Locate and identify every blood parasite.
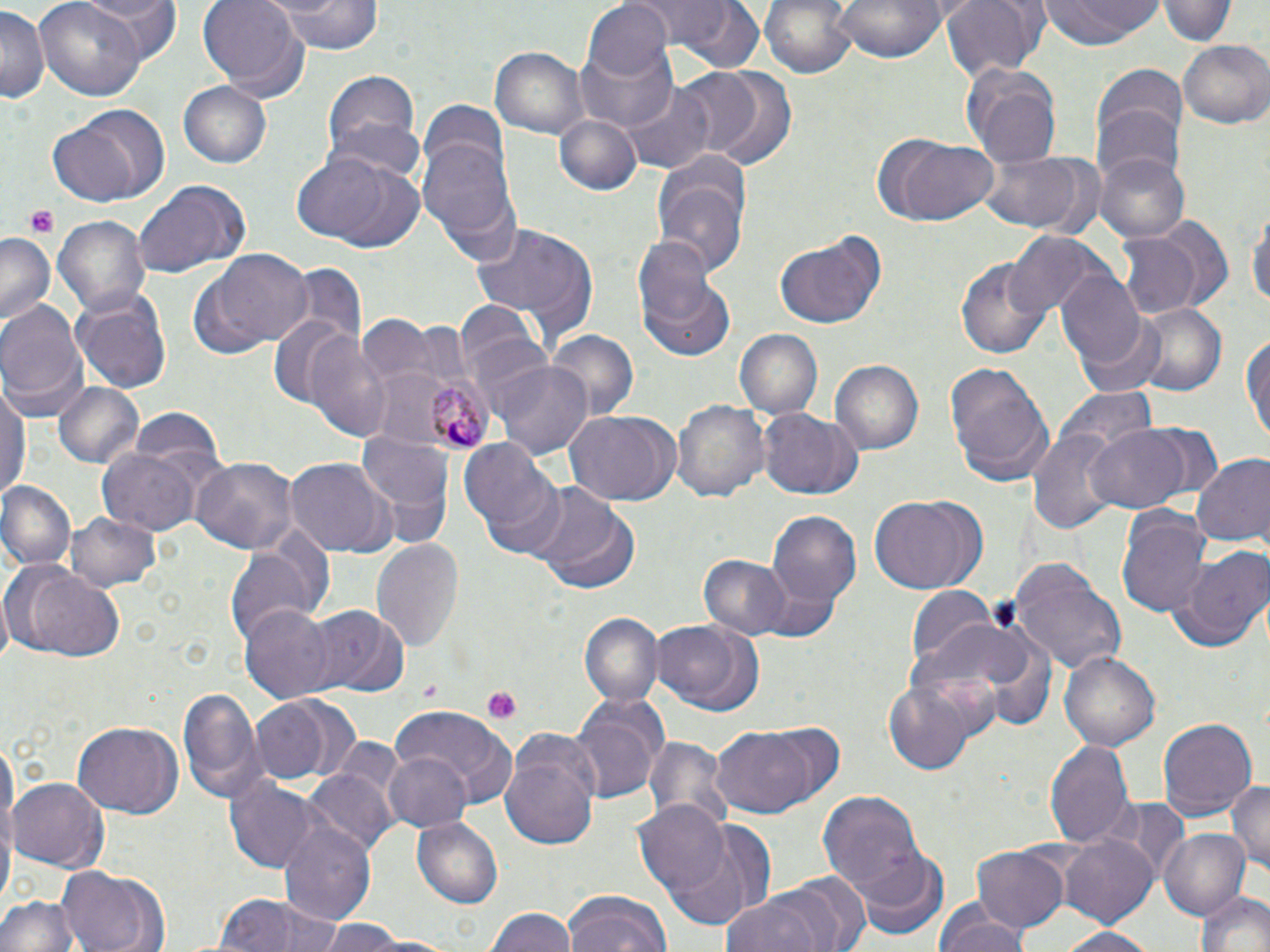

Approximate bounding boxes as [x1, y1, x2, y2] in pixels.
Plasmodium malariae-infected red blood cells: [425, 375, 491, 451].
No Plasmodium falciparum, Plasmodium ovale, Plasmodium vivax, Babesia divergens, or Trypanosoma brucei observed.

Summary:
  - Platelet locations: [25, 205, 61, 236], [478, 685, 525, 726]
  - Uninfected red blood cell locations: [33, 0, 144, 99], [80, 0, 181, 66], [198, 0, 308, 100], [269, 0, 386, 56], [582, 0, 677, 83], [622, 0, 762, 60], [758, 0, 859, 80], [832, 0, 951, 62], [941, 0, 1040, 80], [1040, 0, 1164, 49], [1160, 0, 1236, 47], [0, 9, 45, 102], [577, 40, 680, 132], [1180, 40, 1270, 129], [490, 46, 588, 139], [961, 63, 1061, 164], [674, 66, 767, 158], [1090, 66, 1187, 152], [322, 68, 420, 169], [704, 68, 799, 172], [622, 80, 715, 173], [179, 81, 270, 168], [421, 99, 512, 189], [50, 103, 170, 204], [1091, 105, 1185, 191], [553, 112, 642, 196], [417, 135, 520, 254], [877, 135, 999, 226], [291, 148, 417, 250], [1097, 152, 1192, 244], [977, 153, 1100, 236], [654, 154, 752, 273], [133, 180, 248, 277], [1248, 207, 1269, 321], [54, 215, 151, 320], [1155, 217, 1230, 306], [470, 223, 595, 328], [774, 228, 889, 330], [1116, 232, 1200, 318], [1007, 233, 1106, 323], [0, 235, 53, 324], [633, 237, 718, 327], [198, 250, 314, 351], [954, 254, 1053, 360], [638, 266, 738, 367], [1057, 274, 1146, 367], [72, 292, 172, 396], [0, 299, 86, 414], [456, 301, 547, 386], [1133, 302, 1226, 394], [268, 311, 359, 410], [358, 315, 432, 391], [1073, 315, 1167, 397], [1242, 328, 1270, 449], [737, 329, 823, 418], [546, 330, 637, 421], [307, 332, 389, 440], [491, 359, 593, 459], [832, 360, 922, 456], [946, 362, 1056, 485], [1, 378, 30, 502], [54, 383, 144, 468], [1053, 387, 1156, 456], [671, 397, 771, 506], [130, 406, 225, 478], [757, 409, 861, 500], [564, 412, 679, 504], [1135, 422, 1224, 504], [1028, 424, 1125, 536], [1083, 424, 1192, 514], [356, 430, 452, 535], [460, 437, 568, 560], [98, 447, 199, 536], [191, 456, 300, 554], [1191, 456, 1269, 549], [285, 458, 392, 557], [0, 481, 76, 571], [527, 482, 639, 594], [869, 493, 979, 595], [1117, 505, 1212, 617], [67, 511, 163, 593], [769, 512, 863, 609], [372, 536, 466, 654], [224, 541, 324, 652], [1168, 543, 1268, 652], [700, 554, 794, 638], [1010, 558, 1128, 674], [14, 565, 127, 665], [909, 587, 999, 671], [240, 603, 338, 703], [305, 605, 411, 698], [582, 613, 662, 707], [649, 619, 753, 708], [1059, 648, 1164, 752], [882, 679, 978, 776], [178, 683, 265, 805], [252, 694, 357, 790], [568, 694, 667, 802], [382, 711, 514, 819], [1157, 716, 1256, 821], [72, 719, 181, 819], [708, 723, 824, 819], [644, 732, 733, 832], [1045, 738, 1134, 851], [501, 745, 598, 851], [382, 750, 474, 833], [305, 768, 396, 857], [7, 774, 105, 869], [225, 777, 320, 871], [1227, 777, 1270, 876], [817, 790, 924, 896], [1108, 798, 1189, 888], [634, 800, 733, 897], [278, 815, 376, 927], [412, 818, 505, 909], [669, 826, 769, 931], [1159, 831, 1248, 918], [1059, 833, 1160, 927], [973, 846, 1069, 933], [853, 850, 947, 939], [62, 867, 164, 952], [764, 871, 869, 952], [1198, 887, 1270, 952], [561, 889, 673, 952], [717, 890, 837, 952], [211, 891, 334, 952], [0, 892, 85, 952], [935, 898, 1029, 952], [487, 908, 574, 952], [320, 920, 407, 952], [1053, 924, 1162, 952], [360, 934, 462, 951]
  - Slide-level diagnosis: Plasmodium malariae
  - Magnification: 1000x
  - Image size: 1270×952 pixels
  - Field of view: single
  - Stain: May-Grünwald-Giemsa
  - Preparation: thin blood smear
  - Modality: light microscopy